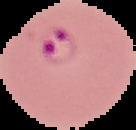

Summary:
  - Result: malaria parasites detected
  - Image type: segmented cell region on a black background
  - Image size: 136×130 pixels
  - Preparation: thin blood smear